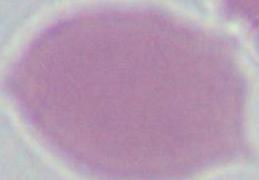
Summary:
  - Modality: photomicrograph
  - Magnification: 1000x
  - Identification: erythrocyte